Give the position of every malaria parasite, noting whether each is a trophozoite, schizont, or gametocyte.
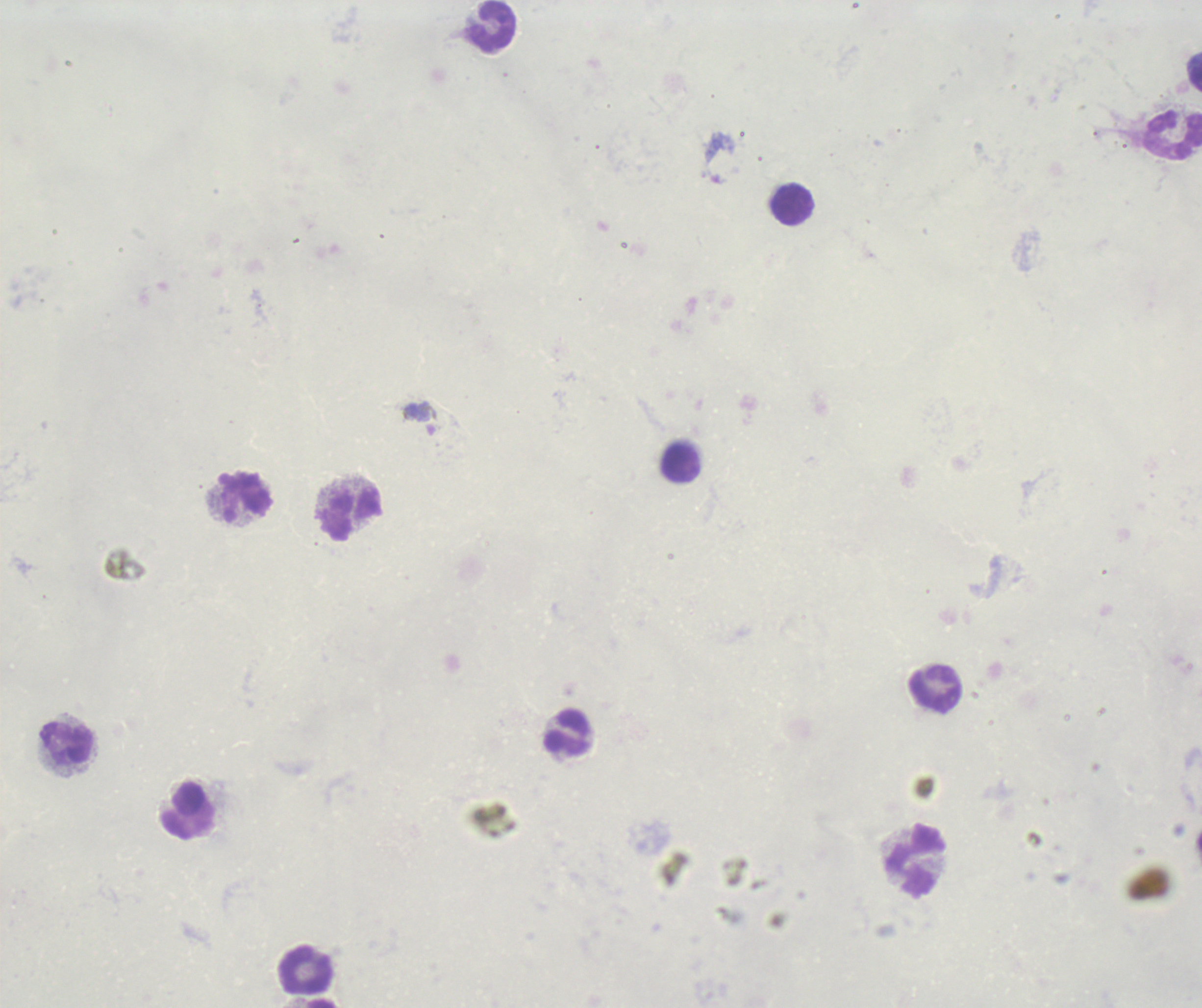
Approximate centers as {x, y} in pixels.
Gametocytes: {419, 419}.
No trophozoite or schizont forms observed.

Approximate centers as {x, y} in pixels. Leukocyte locations: {492, 26}, {1172, 134}, {793, 204}, {680, 463}, {246, 496}, {353, 515}, {935, 689}, {568, 733}, {66, 742}, {183, 811}, {918, 861}, {307, 971}. Background quality: poor. One field from this slide. Thick blood film. Captured at 100x magnification. Previously used in an actual diagnosis. Image is 1202×1008 pixels. Romanowsky-stained preparation.